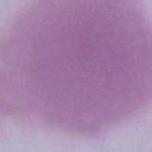

modality = micrograph
identification = red blood cell
magnification = 1000x